Assess this cell for malaria.
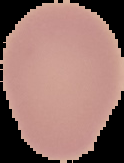
It is uninfected.

Summary:
  - Image type: segmented cell region on a black background
  - Preparation: thin blood smear
  - Image size: 124×163 pixels